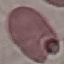 Result: no malaria parasites detected. Cell patch, automatically extracted from a larger field of view and resized to 64 × 64 pixels. Photographed with a smartphone camera at the microscope eyepiece. Thin blood smear. Giemsa-stained preparation.